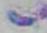
Summary:
  - Modality: micrograph
  - Magnification: 1000x
  - Identification: Toxoplasma gondii